State which parasite is depicted.
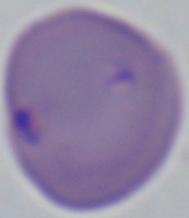
Babesia.

magnification = 1000x
modality = photomicrograph